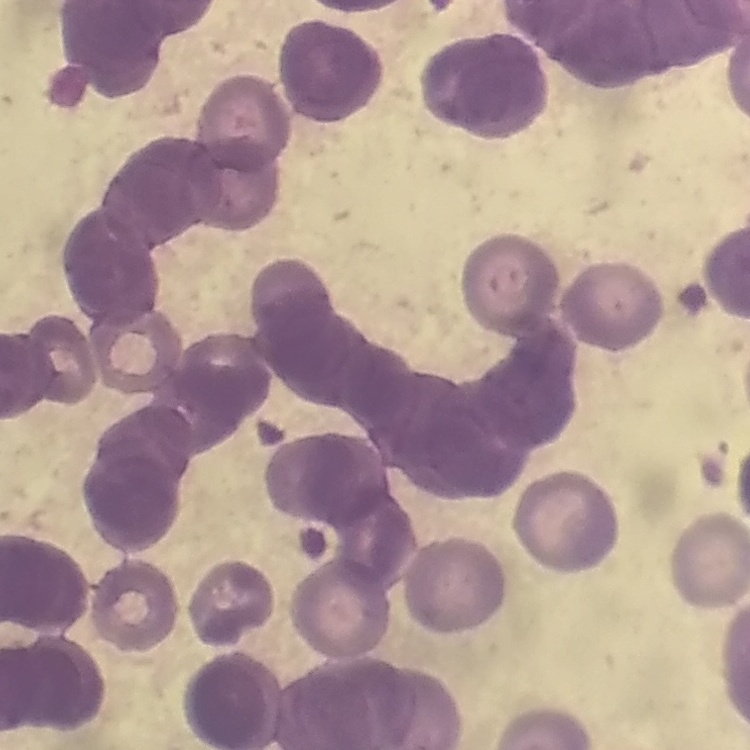
erythrocyte morphology = rouleaux formation
preparation = thin blood smear
image type = square crop of a larger photomicrograph
stain = Field's or Giemsa